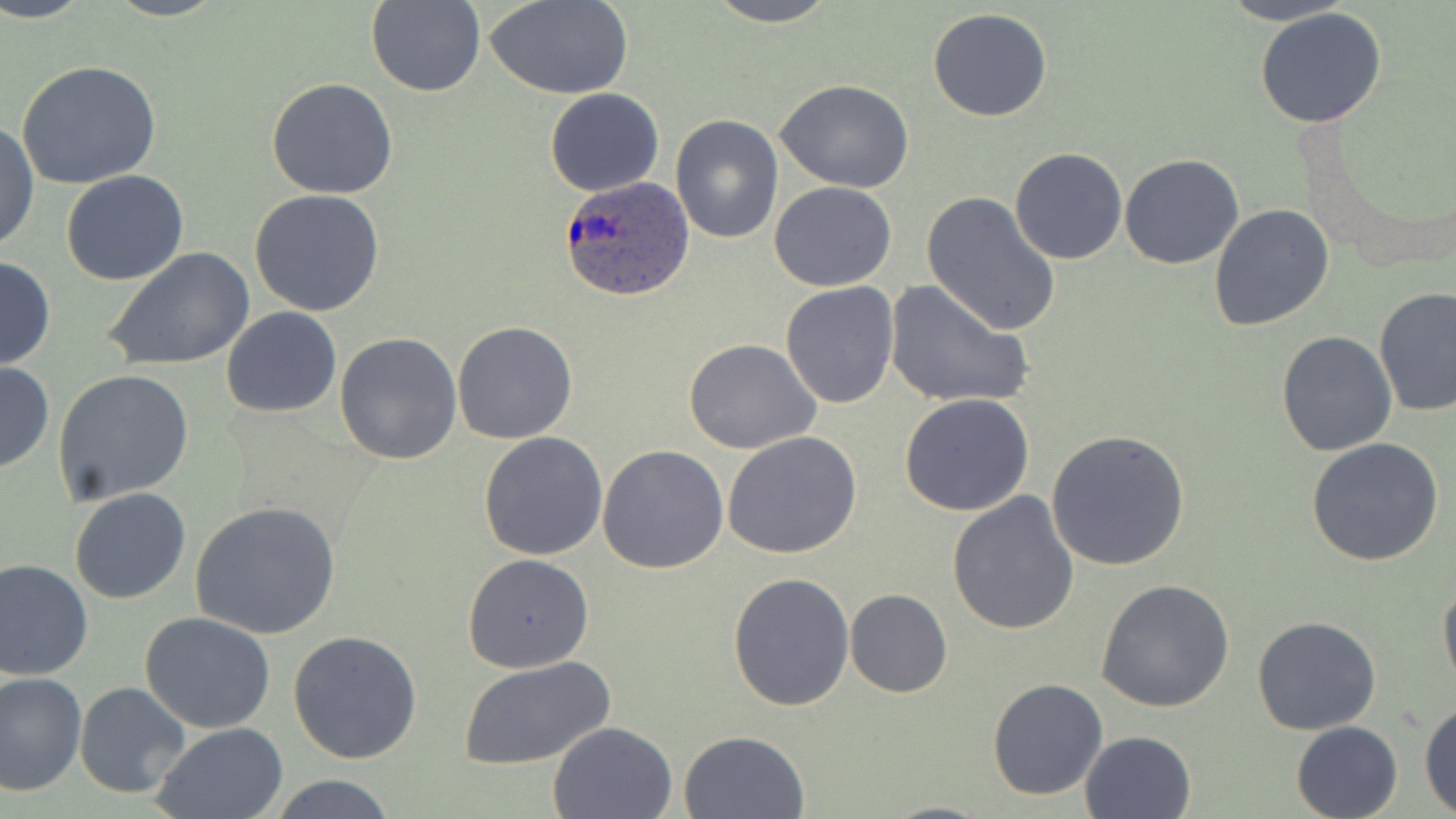
slide_level_diagnosis: Plasmodium ovale
modality: light microscopy
plasmodium_ovale_infected_red_blood_cell_locations: 'approximate bounding boxes as (x1, y1, x2, y2) in pixels: (558, 175, 694, 302)'
field_of_view: one of a larger specimen
image_size: 1456×819 pixels
stain: May-Grünwald-Giemsa
preparation: thin blood smear
magnification: 1000x
uninfected_red_blood_cell_locations: 'approximate bounding boxes as (x1, y1, x2, y2) in pixels: (0, 0, 95, 24), (487, 0, 634, 99), (704, 0, 842, 27), (1214, 0, 1358, 25), (365, 1, 486, 97), (927, 8, 1053, 122), (1255, 9, 1388, 128), (16, 59, 161, 190), (265, 78, 398, 200), (774, 80, 916, 193), (545, 88, 665, 198), (670, 114, 783, 245), (0, 119, 38, 254), (1009, 147, 1127, 264), (1120, 153, 1244, 270), (61, 169, 188, 286), (769, 181, 897, 292), (250, 189, 386, 317), (920, 193, 1061, 338), (1208, 202, 1334, 334), (103, 246, 256, 374), (0, 255, 55, 371), (882, 278, 1033, 411), (781, 281, 898, 408), (1376, 287, 1456, 416), (220, 307, 341, 418), (452, 320, 579, 445), (1277, 331, 1398, 457), (334, 333, 462, 466), (682, 338, 821, 455), (0, 361, 53, 472), (53, 369, 194, 508), (901, 392, 1035, 516), (1045, 428, 1190, 570), (477, 431, 607, 561), (721, 431, 862, 558), (1305, 439, 1445, 568), (598, 445, 728, 573), (69, 487, 193, 604), (945, 490, 1079, 635), (191, 500, 342, 638), (463, 553, 595, 673), (0, 557, 94, 681), (727, 571, 855, 712), (1438, 577, 1456, 694), (1095, 579, 1235, 712), (844, 588, 951, 698), (140, 611, 276, 733), (1252, 617, 1382, 736), (288, 628, 422, 763), (460, 655, 615, 769), (0, 670, 86, 795), (988, 678, 1108, 801), (75, 682, 190, 798), (1418, 699, 1456, 815), (548, 719, 679, 818), (1291, 721, 1403, 818), (149, 723, 288, 818), (679, 729, 809, 817), (1079, 730, 1198, 819), (268, 775, 400, 818), (882, 799, 996, 818)'